Report the malaria status of this cell.
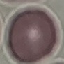
Uninfected.

{
  "capture": "smartphone through the microscope eyepiece",
  "preparation": "thin blood film",
  "image_type": "automatically extracted cell patch, resized to 64 × 64 pixels",
  "stain": "Giemsa"
}